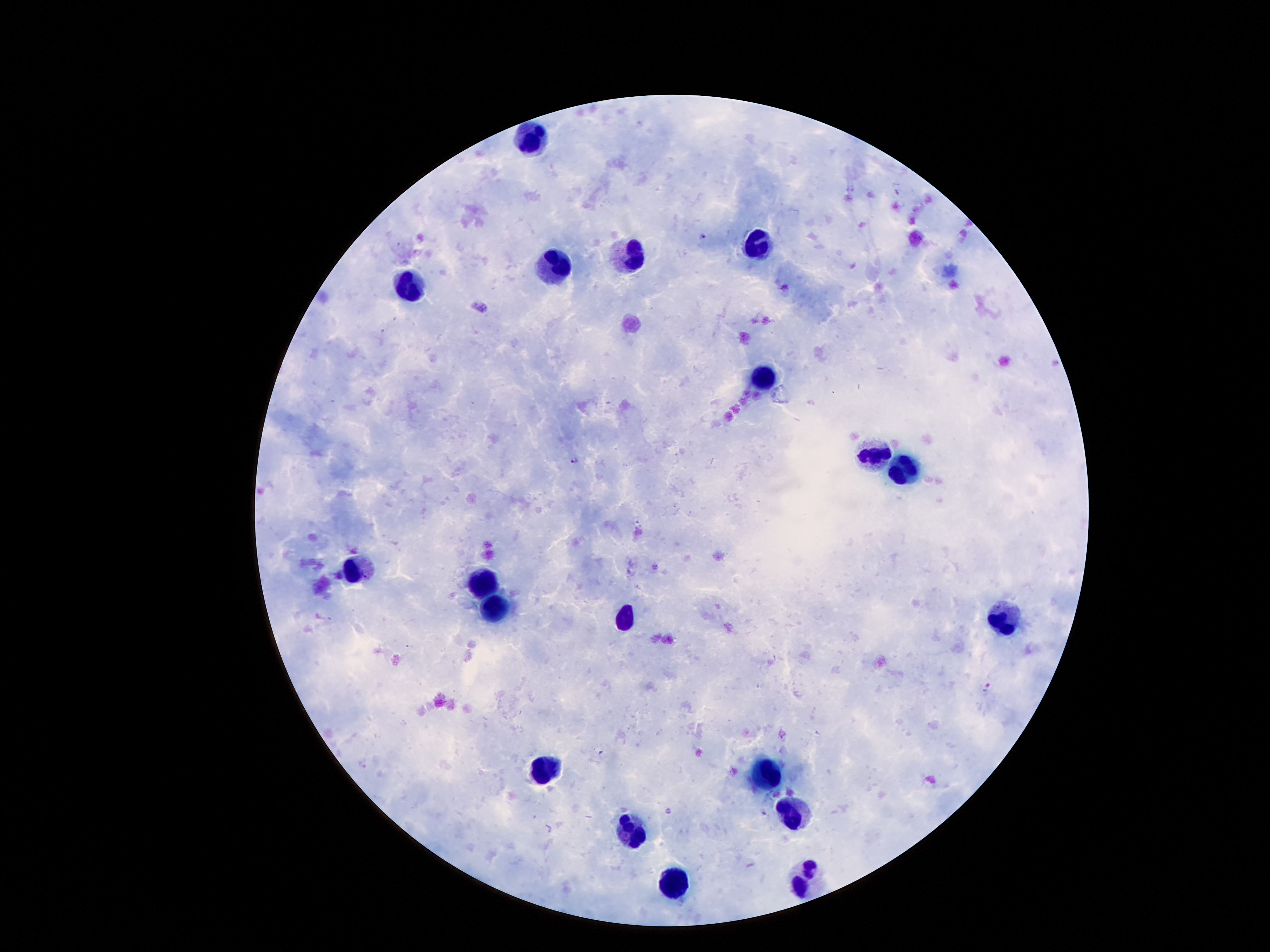
Approximate centers as (x, y) in pixels.
Summary:
  - Malaria parasite locations: (851, 187), (897, 193), (702, 233), (574, 459), (988, 686), (603, 754), (764, 811)
  - Leukocyte locations: (524, 138), (751, 247), (628, 260), (556, 265), (408, 292), (765, 378), (871, 451), (903, 469), (358, 570), (481, 580), (497, 605), (1003, 619), (624, 621), (547, 767), (765, 771), (792, 814), (628, 835), (806, 872), (674, 885)
  - Capture: smartphone through the microscope eyepiece
  - Magnification: 100x
  - Stain: Giemsa
  - Preparation: thick blood smear
  - Image size: 1270×952 pixels
  - Field of view: one from this slide
  - Patient malaria status: positive for Plasmodium falciparum